Assess the morphology of the erythrocytes.
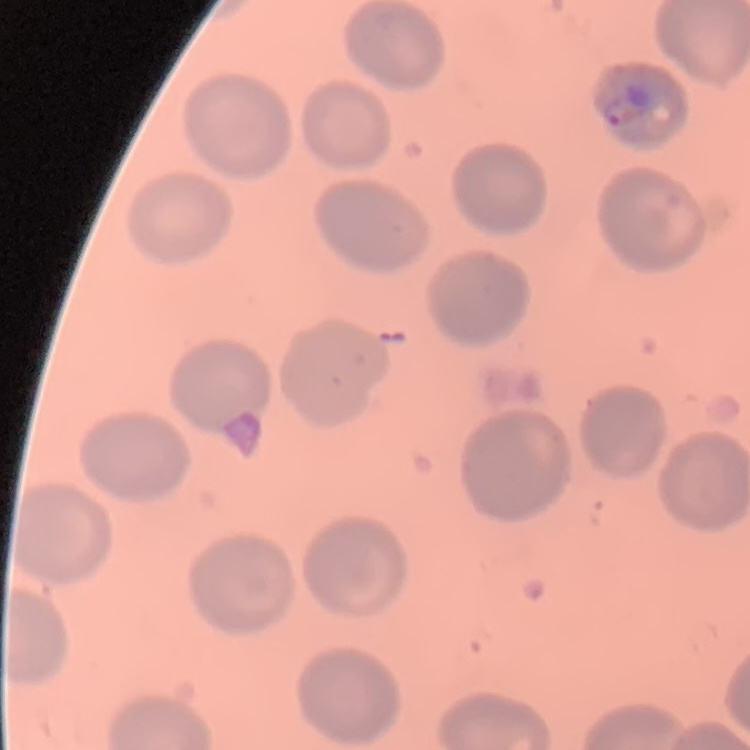
They show no rouleaux formation.

preparation: thin blood smear
stain: Field's or Giemsa
image_type: square crop of a larger photomicrograph